Comment on the morphology of the red blood cells.
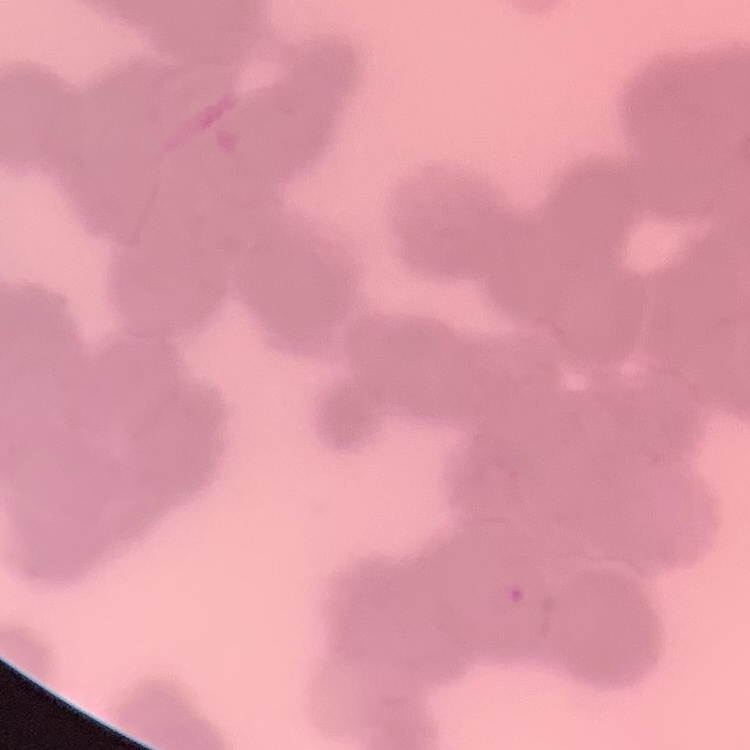

They show rouleaux formation.

stain = Field's or Giemsa
preparation = thin peripheral smear
image type = square crop of a larger photomicrograph